Locate every blood parasite and identify its species.
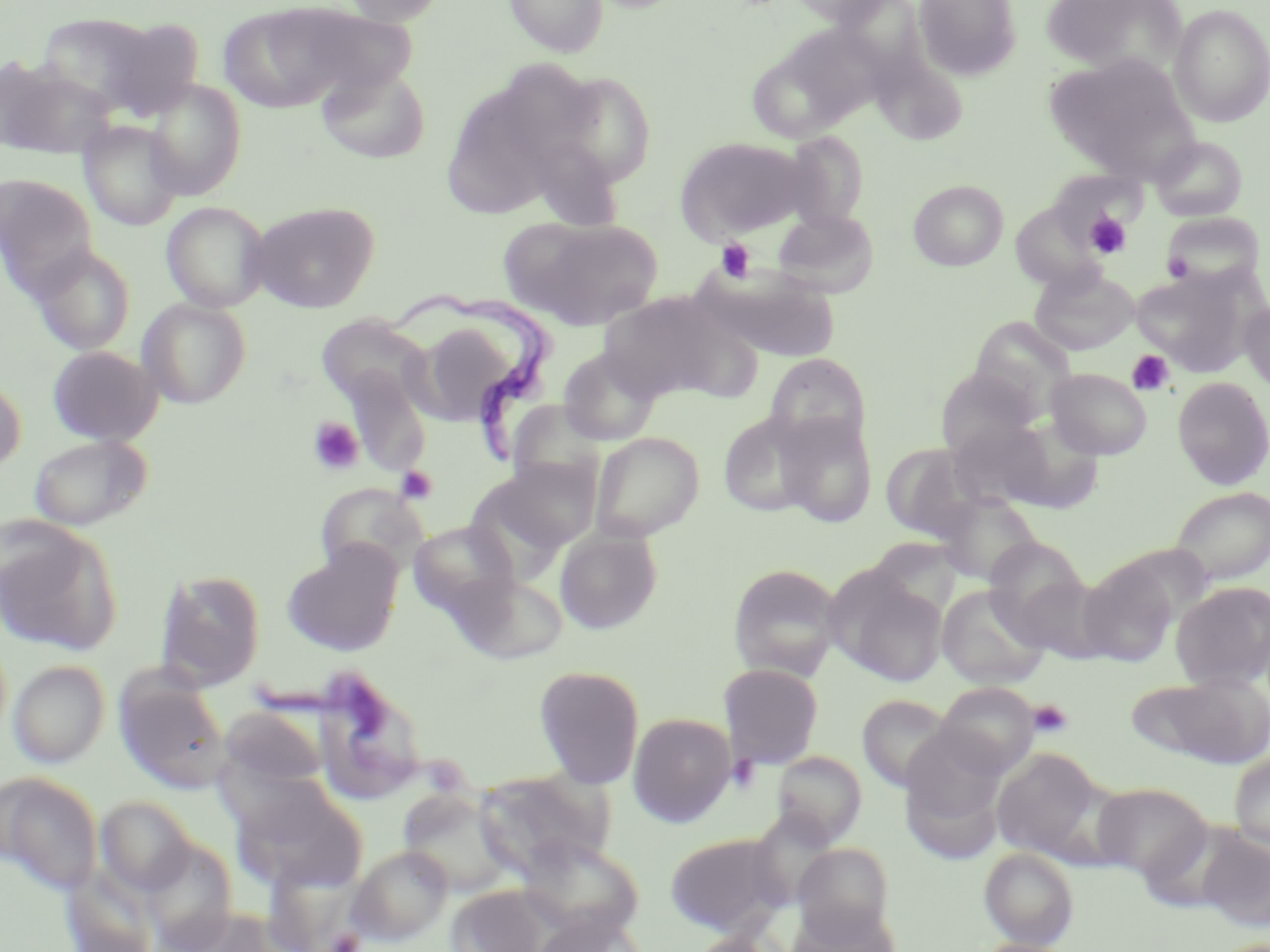

Approximate bounding boxes as named x1/y1/x2/y2 corners in pixels.
Trypanosoma brucei: (x1=388, y1=290, x2=555, y2=462).
No Plasmodium falciparum, Plasmodium ovale, Plasmodium malariae, Plasmodium vivax, or Babesia divergens observed.

Platelet locations: (x1=1083, y1=211, x2=1132, y2=260), (x1=715, y1=239, x2=755, y2=283), (x1=1161, y1=252, x2=1194, y2=281), (x1=1127, y1=350, x2=1174, y2=396), (x1=308, y1=416, x2=365, y2=476), (x1=396, y1=466, x2=437, y2=504), (x1=1027, y1=699, x2=1073, y2=739), (x1=326, y1=929, x2=364, y2=951). Uninfected red blood cell locations: (x1=219, y1=0, x2=407, y2=112), (x1=342, y1=0, x2=449, y2=26), (x1=504, y1=0, x2=609, y2=58), (x1=782, y1=0, x2=893, y2=25), (x1=825, y1=0, x2=931, y2=75), (x1=913, y1=0, x2=1022, y2=81), (x1=1041, y1=0, x2=1185, y2=77), (x1=1169, y1=3, x2=1270, y2=128), (x1=37, y1=12, x2=169, y2=114), (x1=97, y1=17, x2=205, y2=120), (x1=755, y1=22, x2=889, y2=138), (x1=1044, y1=52, x2=1198, y2=183), (x1=315, y1=63, x2=431, y2=164), (x1=1, y1=65, x2=117, y2=159), (x1=553, y1=71, x2=659, y2=187), (x1=144, y1=80, x2=247, y2=200), (x1=440, y1=83, x2=566, y2=219), (x1=79, y1=120, x2=184, y2=231), (x1=781, y1=131, x2=871, y2=230), (x1=1149, y1=134, x2=1248, y2=222), (x1=675, y1=136, x2=810, y2=243), (x1=0, y1=175, x2=98, y2=290), (x1=907, y1=179, x2=1009, y2=271), (x1=161, y1=201, x2=271, y2=312), (x1=249, y1=202, x2=380, y2=313), (x1=772, y1=208, x2=879, y2=297), (x1=1159, y1=212, x2=1266, y2=293), (x1=508, y1=218, x2=664, y2=329), (x1=30, y1=245, x2=135, y2=355), (x1=1029, y1=264, x2=1140, y2=355), (x1=1130, y1=264, x2=1261, y2=376), (x1=699, y1=267, x2=841, y2=362), (x1=598, y1=291, x2=751, y2=404), (x1=138, y1=298, x2=251, y2=408), (x1=1239, y1=300, x2=1270, y2=395), (x1=316, y1=314, x2=431, y2=412), (x1=414, y1=314, x2=539, y2=424), (x1=969, y1=317, x2=1078, y2=420), (x1=47, y1=345, x2=161, y2=446), (x1=557, y1=347, x2=662, y2=446), (x1=764, y1=354, x2=871, y2=451), (x1=339, y1=366, x2=432, y2=476), (x1=935, y1=368, x2=1040, y2=463), (x1=1045, y1=368, x2=1153, y2=460), (x1=0, y1=372, x2=26, y2=475), (x1=1172, y1=376, x2=1270, y2=489), (x1=506, y1=400, x2=610, y2=496), (x1=717, y1=410, x2=821, y2=519), (x1=775, y1=412, x2=879, y2=527), (x1=990, y1=413, x2=1106, y2=514), (x1=590, y1=431, x2=704, y2=541), (x1=27, y1=434, x2=151, y2=531), (x1=881, y1=442, x2=987, y2=543), (x1=489, y1=457, x2=601, y2=552), (x1=315, y1=483, x2=428, y2=577), (x1=1169, y1=486, x2=1270, y2=586), (x1=935, y1=491, x2=1044, y2=586), (x1=0, y1=520, x2=121, y2=656), (x1=408, y1=521, x2=520, y2=617), (x1=555, y1=529, x2=662, y2=634), (x1=983, y1=537, x2=1092, y2=645), (x1=282, y1=546, x2=402, y2=656), (x1=1079, y1=560, x2=1178, y2=667), (x1=728, y1=563, x2=843, y2=681), (x1=155, y1=568, x2=266, y2=691), (x1=829, y1=568, x2=948, y2=688), (x1=451, y1=571, x2=568, y2=663), (x1=1013, y1=573, x2=1117, y2=664), (x1=1170, y1=581, x2=1270, y2=690), (x1=936, y1=585, x2=1049, y2=690), (x1=8, y1=660, x2=110, y2=768), (x1=718, y1=663, x2=824, y2=768), (x1=533, y1=665, x2=645, y2=789), (x1=115, y1=673, x2=233, y2=795), (x1=1132, y1=673, x2=1270, y2=768), (x1=933, y1=682, x2=1041, y2=779), (x1=856, y1=694, x2=957, y2=794), (x1=221, y1=706, x2=329, y2=788), (x1=628, y1=712, x2=736, y2=827), (x1=899, y1=738, x2=1009, y2=866), (x1=991, y1=748, x2=1107, y2=861), (x1=771, y1=750, x2=867, y2=846), (x1=1230, y1=752, x2=1270, y2=851), (x1=474, y1=769, x2=614, y2=880), (x1=0, y1=771, x2=103, y2=896), (x1=234, y1=779, x2=367, y2=893), (x1=1092, y1=782, x2=1211, y2=883), (x1=397, y1=789, x2=514, y2=897), (x1=95, y1=796, x2=195, y2=897), (x1=1195, y1=828, x2=1270, y2=932), (x1=665, y1=832, x2=789, y2=937), (x1=517, y1=835, x2=645, y2=941), (x1=141, y1=837, x2=238, y2=951), (x1=792, y1=843, x2=894, y2=941), (x1=346, y1=845, x2=452, y2=946), (x1=979, y1=847, x2=1079, y2=949), (x1=62, y1=868, x2=159, y2=952), (x1=446, y1=885, x2=551, y2=951), (x1=783, y1=906, x2=898, y2=952), (x1=530, y1=912, x2=646, y2=952), (x1=679, y1=933, x2=792, y2=952). Slide-level diagnosis: Trypanosoma brucei. Thin blood smear. Light microscopy. May-Grünwald-Giemsa-stained preparation. One field of a larger specimen. Captured at 1000x magnification. Image is 1270×952 pixels.